Identify the cell.
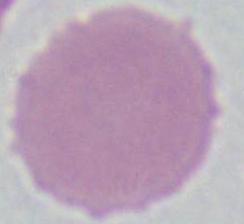
This is an erythrocyte.

modality = micrograph
magnification = 1000x